Assess the morphology of the erythrocytes.
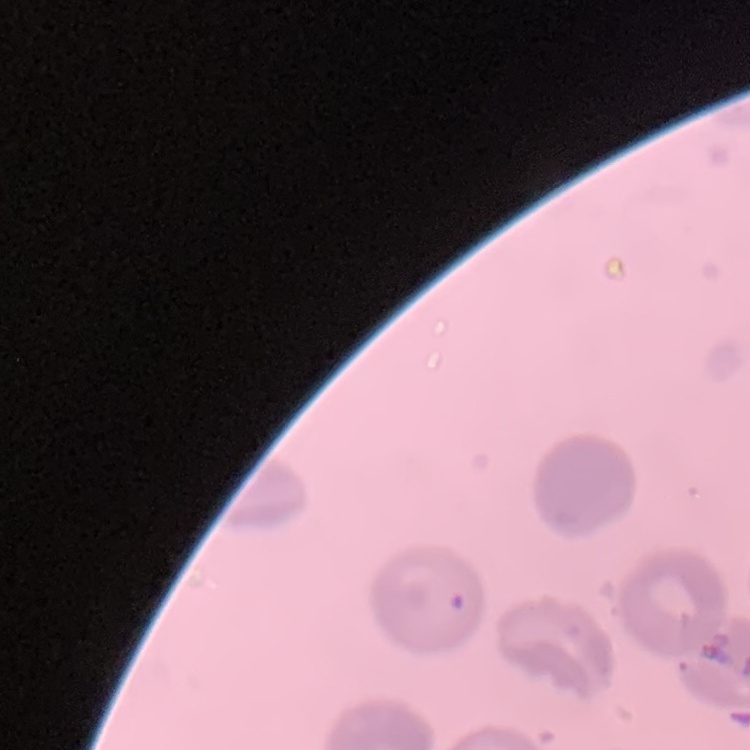
No rouleaux formation.

preparation = thin peripheral smear
image type = one tile cut from a larger photomicrograph
stain = Field's or Giemsa